Assess the morphology of the red blood cells.
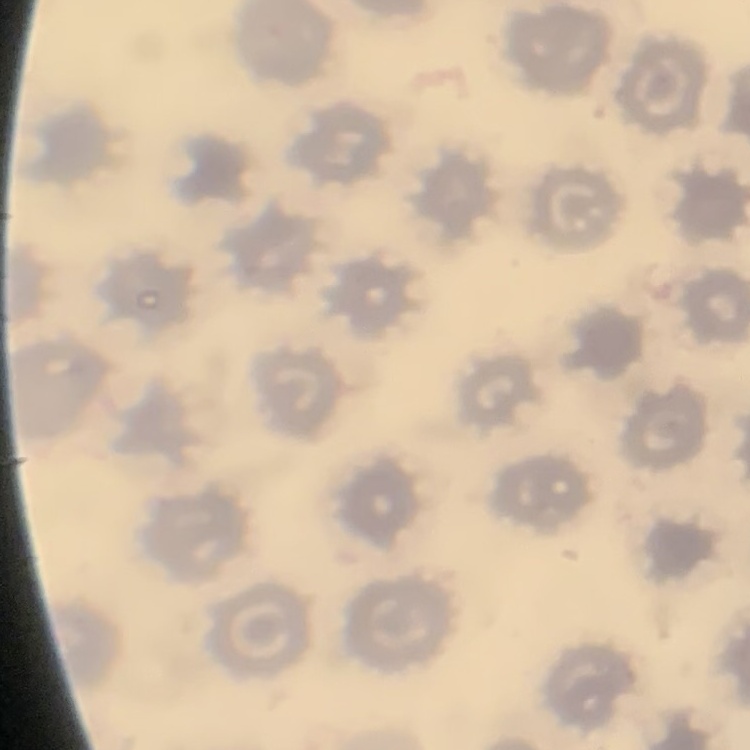

No rouleaux formation.

preparation = thin blood smear
image type = one tile cut from a larger photomicrograph
stain = Field's or Giemsa